Point out each leukocyte.
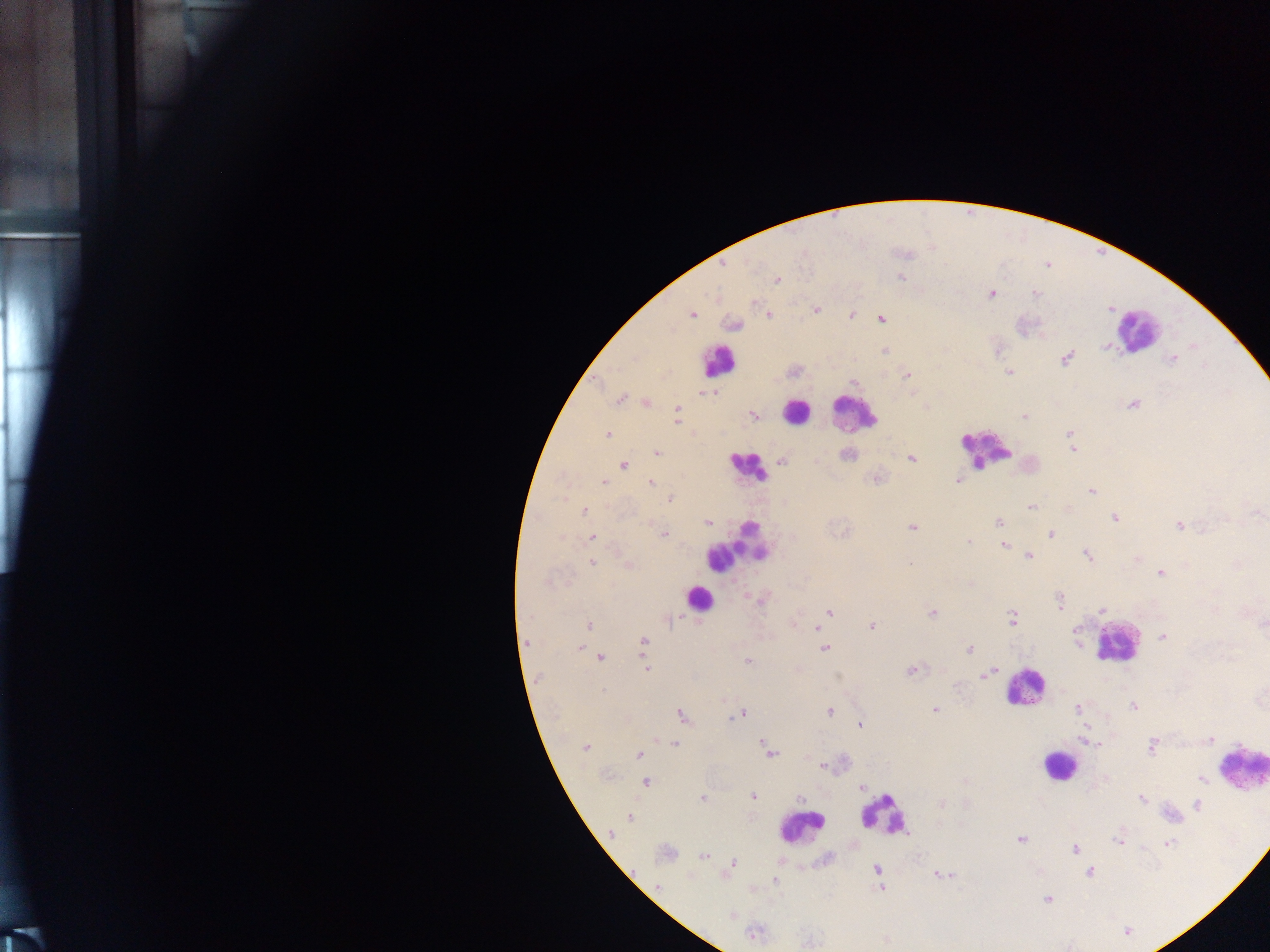
Approximate centers as {x, y} in pixels.
Leukocytes: {1137, 330}, {719, 361}, {796, 411}, {853, 414}, {983, 448}, {747, 466}, {737, 545}, {699, 599}, {1117, 642}, {1024, 688}, {1058, 765}, {1240, 766}, {882, 815}, {801, 828}.

Malaria parasite locations: {723, 264}, {900, 276}, {777, 279}, {991, 293}, {1035, 293}, {816, 309}, {691, 314}, {768, 314}, {851, 315}, {880, 318}, {733, 324}, {1106, 346}, {884, 352}, {1066, 357}, {1172, 358}, {1010, 371}, {908, 376}, {854, 382}, {708, 392}, {718, 392}, {619, 399}, {645, 402}, {1133, 403}, {926, 407}, {677, 412}, {753, 414}, {1025, 416}, {1069, 433}, {606, 435}, {1073, 449}, {657, 453}, {847, 454}, {911, 458}, {781, 461}, {623, 464}, {877, 478}, {958, 480}, {603, 482}, {650, 482}, {1090, 490}, {670, 498}, {1031, 506}, {1067, 507}, {584, 511}, {1114, 518}, {708, 522}, {997, 522}, {1179, 525}, {912, 527}, {663, 534}, {1050, 534}, {591, 537}, {968, 542}, {1004, 545}, {1028, 556}, {1087, 556}, {1137, 558}, {592, 562}, {627, 565}, {1237, 565}, {1161, 573}, {970, 583}, {762, 598}, {1059, 600}, {1101, 609}, {829, 612}, {932, 613}, {1011, 619}, {793, 623}, {1262, 624}, {589, 625}, {871, 626}, {816, 628}, {1163, 637}, {643, 641}, {526, 643}, {1077, 643}, {824, 647}, {580, 648}, {969, 648}, {600, 657}, {748, 661}, {645, 669}, {911, 669}, {994, 671}, {982, 674}, {1133, 706}, {1077, 707}, {934, 709}, {828, 711}, {740, 713}, {682, 715}, {860, 724}, {1084, 726}, {1206, 740}, {761, 741}, {674, 743}, {1098, 743}, {1152, 745}, {586, 747}, {770, 752}, {638, 754}, {822, 765}, {1201, 778}, {646, 781}, {861, 786}, {753, 796}, {798, 797}, {702, 799}, {1141, 799}, {941, 804}, {1197, 805}, {630, 817}, {611, 834}, {1020, 839}, {1120, 842}, {1167, 843}, {1074, 849}, {665, 852}, {704, 856}, {732, 861}, {877, 869}, {1089, 871}, {725, 874}, {939, 875}, {774, 880}, {656, 887}, {882, 887}, {1048, 898}, {731, 915}, {754, 934}, {885, 939}. Image is 1270×952 pixels. Thick blood film. Collected in Ghana. One field of view. Mobile-phone photograph taken through the microscope.